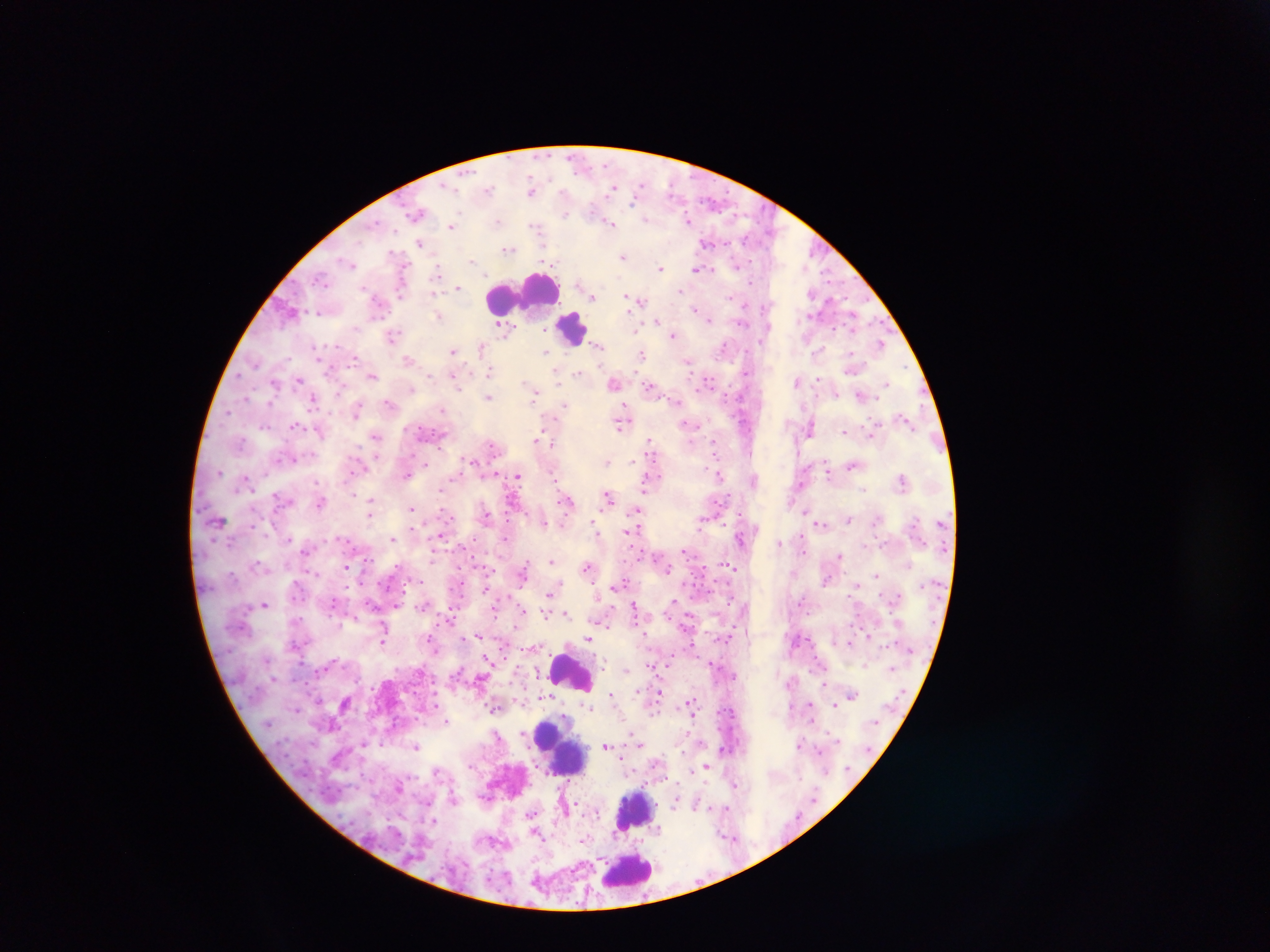
{
  "plasmodium_parasite_locations": "approximate centers as [x, y] in pixels: [615, 187], [531, 189], [417, 213], [689, 220], [612, 223], [452, 226], [708, 242], [421, 243], [508, 248], [623, 256], [661, 268], [698, 269], [438, 271], [458, 287], [681, 290], [593, 296], [635, 300], [291, 310], [699, 310], [438, 316], [707, 318], [658, 322], [503, 326], [393, 334], [674, 335], [881, 344], [598, 346], [482, 348], [454, 351], [545, 352], [641, 354], [409, 360], [689, 361], [853, 366], [489, 371], [557, 372], [578, 372], [372, 375], [454, 377], [299, 378], [614, 382], [709, 382], [798, 382], [275, 383], [887, 384], [651, 387], [534, 392], [861, 395], [489, 397], [314, 401], [390, 403], [565, 405], [357, 409], [441, 410], [905, 420], [621, 423], [688, 424], [295, 425], [811, 427], [321, 431], [845, 431], [872, 431], [376, 436], [538, 441], [549, 442], [650, 443], [470, 460], [607, 462], [854, 465], [829, 470], [406, 474], [719, 474], [517, 476], [246, 479], [754, 479], [902, 480], [649, 481], [279, 497], [608, 497], [369, 501], [567, 501], [321, 502], [411, 508], [807, 510], [638, 511], [370, 513], [486, 515], [848, 519], [702, 521], [543, 523], [595, 524], [821, 524], [630, 531], [440, 536], [504, 537], [289, 538], [741, 538], [392, 539], [780, 542], [307, 549], [686, 550], [839, 557], [551, 560], [730, 565], [347, 566], [588, 566], [523, 572], [877, 575], [620, 584], [549, 593], [673, 601], [264, 604], [635, 607], [523, 611], [546, 614], [566, 614], [450, 620], [602, 622], [644, 632], [479, 636], [869, 636], [589, 637], [384, 641], [851, 642], [488, 659], [652, 664], [626, 670], [659, 693], [611, 694], [852, 695], [545, 696], [346, 703], [691, 704], [810, 704], [835, 704], [589, 707], [494, 708], [447, 721], [639, 742], [800, 744], [416, 746], [606, 746], [820, 750], [707, 766], [734, 783], [399, 786], [677, 800], [697, 804], [726, 807], [434, 821], [535, 831], [584, 839]",
  "country": "Ghana",
  "preparation": "thick blood smear",
  "capture": "mobile-phone photograph through a microscope",
  "image_size": "1270×952 pixels",
  "field_of_view": "single",
  "leukocyte_locations": "approximate centers as [x, y] in pixels: [525, 293], [573, 328], [572, 672], [560, 746], [634, 811], [627, 871]"
}